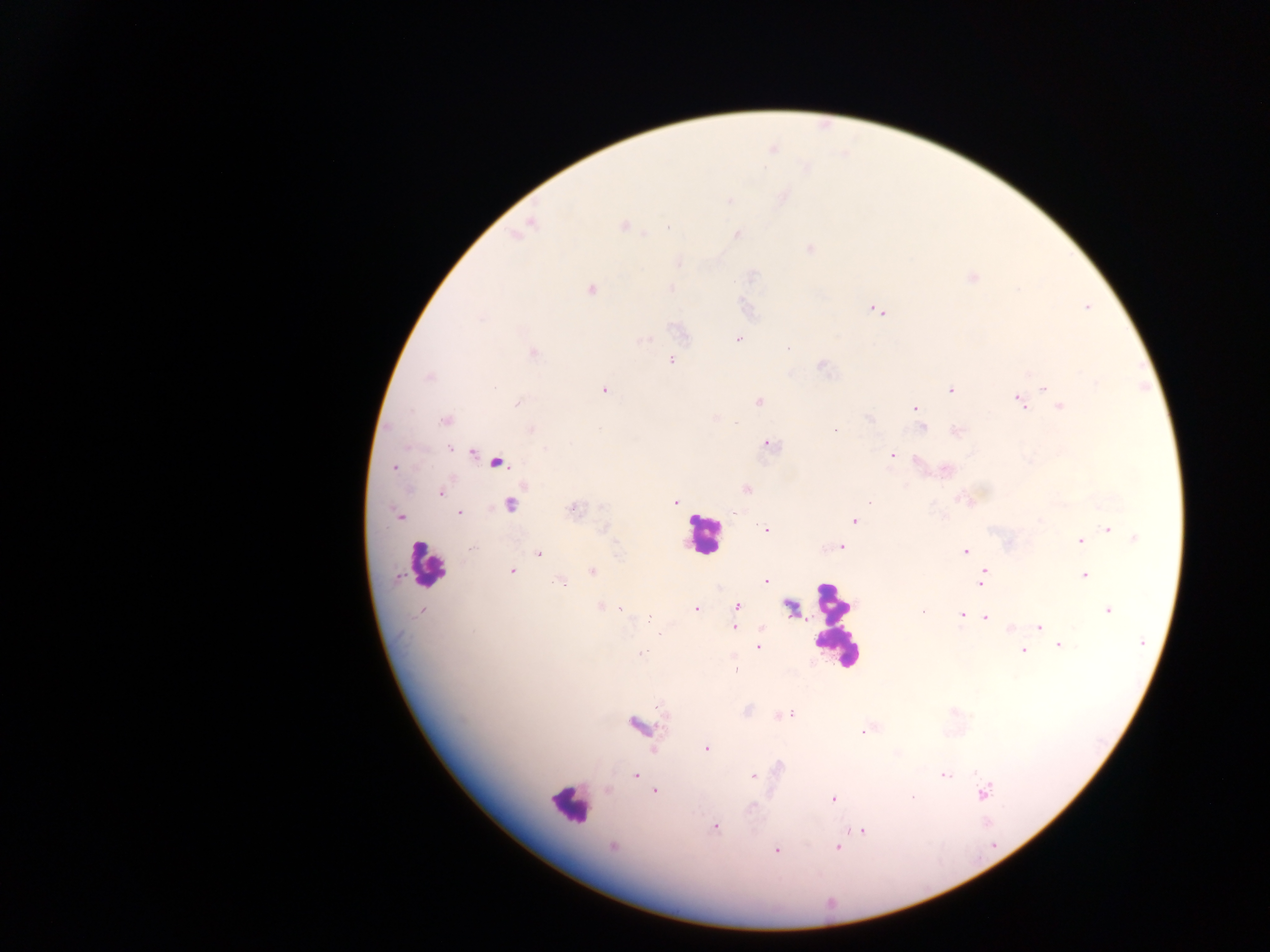
capture = mobile-phone photograph through a microscope
field of view = single
country = Ghana
leukocyte locations = approximate centers as {x, y} in pixels: {703, 535}, {427, 564}, {835, 625}, {568, 805}
image size = 1270×952 pixels
preparation = thick blood smear
Plasmodium parasite locations = approximate centers as {x, y} in pixels: {729, 200}, {530, 223}, {623, 225}, {646, 233}, {737, 234}, {810, 248}, {678, 262}, {971, 278}, {671, 288}, {591, 289}, {1086, 307}, {875, 310}, {679, 330}, {738, 339}, {644, 340}, {787, 348}, {534, 353}, {671, 360}, {821, 366}, {429, 377}, {1096, 382}, {493, 387}, {1044, 388}, {604, 390}, {951, 390}, {758, 401}, {1018, 401}, {517, 403}, {1060, 407}, {914, 408}, {870, 419}, {445, 420}, {923, 427}, {531, 429}, {835, 430}, {956, 432}, {770, 445}, {449, 449}, {473, 453}, {892, 454}, {497, 463}, {394, 467}, {946, 470}, {746, 489}, {441, 492}, {960, 499}, {869, 500}, {676, 501}, {511, 504}, {572, 510}, {459, 513}, {398, 515}, {854, 520}, {765, 529}, {1108, 529}, {1135, 539}, {1080, 541}, {840, 547}, {473, 548}, {965, 551}, {539, 553}, {511, 571}, {592, 571}, {983, 571}, {1085, 576}, {558, 581}, {765, 581}, {980, 582}, {600, 607}, {737, 607}, {789, 607}, {620, 609}, {696, 609}, {1108, 610}, {421, 611}, {922, 612}, {961, 615}, {986, 617}, {648, 618}, {1039, 626}, {734, 627}, {1010, 628}, {1142, 643}, {1060, 645}, {758, 648}, {1023, 650}, {641, 654}, {736, 670}, {788, 714}, {639, 725}, {863, 732}, {706, 749}, {945, 775}, {636, 776}, {753, 776}, {608, 790}, {655, 792}, {985, 793}, {913, 796}, {833, 799}, {751, 807}, {716, 827}, {860, 832}, {612, 847}, {837, 847}, {776, 850}